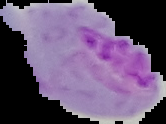
image type = segmented cell region on a black background
image size = 166×124 pixels
malaria status = parasitized
preparation = thin blood film